Report the malaria status of this cell.
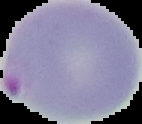

Parasitized.

Summary:
  - Image type: cell region segmented out of the field of view; surrounding area masked to black
  - Image size: 142×124 pixels
  - Preparation: thin blood smear